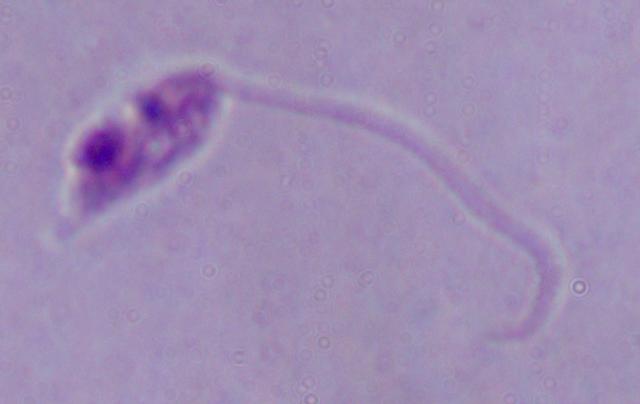
1000x magnification. Photomicrograph. A Leishmania parasite is seen.